Locate every Plasmodium falciparum-infected red blood cell.
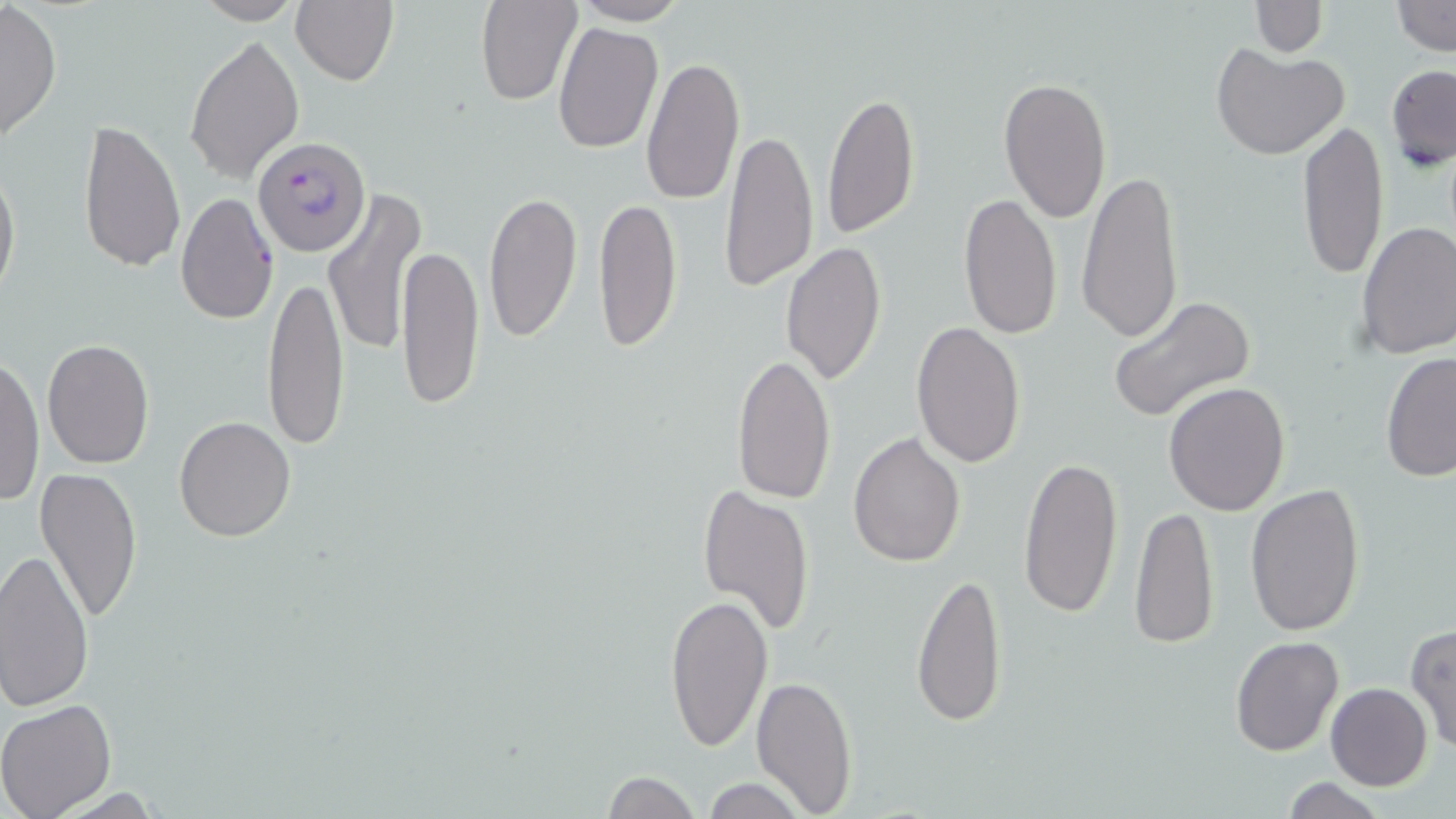

Approximate bounding boxes as [x1, y1, x2, y2] in pixels.
Plasmodium falciparum-infected red blood cells: [253, 137, 372, 257].

Uninfected red blood cell locations: [475, 0, 583, 106], [1233, 0, 1339, 89], [188, 1, 306, 25], [289, 1, 399, 85], [571, 1, 691, 26], [1250, 1, 1326, 56], [1393, 1, 1455, 55], [0, 2, 62, 143], [552, 21, 664, 154], [184, 34, 305, 186], [1213, 43, 1350, 160], [640, 54, 745, 206], [1385, 64, 1456, 171], [997, 76, 1112, 223], [821, 89, 920, 239], [78, 116, 185, 272], [1298, 120, 1388, 282], [721, 125, 819, 295], [0, 154, 21, 310], [1077, 168, 1185, 346], [323, 187, 425, 357], [483, 189, 584, 342], [175, 192, 279, 325], [957, 192, 1060, 341], [593, 193, 682, 352], [1356, 220, 1456, 358], [781, 241, 888, 387], [398, 243, 485, 410], [262, 273, 349, 451], [1108, 296, 1257, 425], [911, 321, 1027, 469], [41, 338, 155, 470], [1381, 350, 1456, 483], [731, 352, 837, 504], [0, 355, 46, 505], [1163, 382, 1290, 517], [174, 417, 296, 541], [848, 431, 965, 566], [1018, 453, 1125, 619], [34, 464, 142, 626], [1244, 484, 1367, 638], [697, 485, 815, 638], [1130, 506, 1219, 651], [0, 549, 96, 713], [914, 571, 1008, 730], [665, 593, 773, 752], [1405, 623, 1455, 755], [1230, 635, 1344, 756], [750, 674, 859, 816], [1325, 682, 1433, 790], [0, 699, 118, 819], [601, 770, 700, 819], [697, 777, 810, 819], [1278, 778, 1391, 818]. Slide-level diagnosis: Plasmodium falciparum. Image is 1456×819 pixels. May-Grünwald-Giemsa stain. 1000x magnification. Single field of view. Thin blood film. Light microscopy.